Assess this cell for malaria.
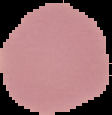
It is uninfected.

Image is 112×115 pixels. Segmented cell region on a black background. From a thin blood film.